Locate every blood parasite and identify its species.
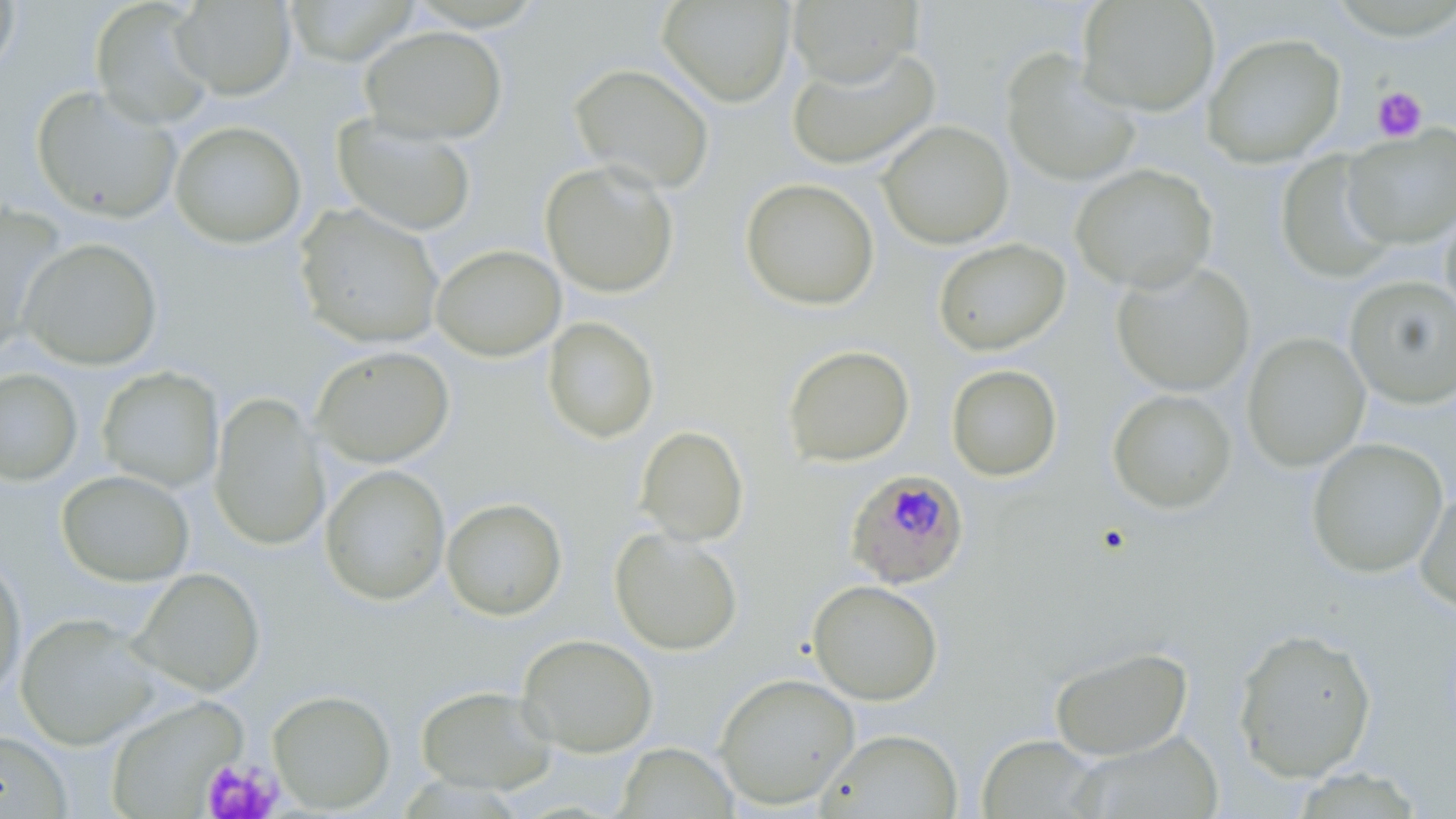
Approximate bounding boxes as (x1, y1, x2, y2) in pixels.
Plasmodium falciparum-infected red blood cells: (845, 469, 971, 590).
No Plasmodium ovale, Plasmodium malariae, Plasmodium vivax, Babesia divergens, or Trypanosoma brucei observed.

Summary:
  - Uninfected red blood cell locations: (0, 0, 21, 82), (90, 0, 216, 130), (657, 0, 795, 107), (787, 0, 922, 88), (170, 1, 297, 100), (1076, 1, 1220, 116), (282, 2, 421, 67), (359, 25, 508, 144), (1202, 31, 1346, 167), (786, 46, 940, 170), (1000, 50, 1142, 187), (569, 63, 715, 194), (30, 85, 182, 224), (332, 115, 477, 236), (169, 120, 307, 249), (877, 120, 1014, 249), (1342, 125, 1456, 249), (1276, 151, 1399, 283), (540, 159, 679, 298), (1069, 163, 1218, 294), (740, 177, 880, 311), (1440, 202, 1456, 325), (294, 204, 445, 350), (1, 205, 66, 356), (18, 238, 163, 370), (933, 238, 1070, 356), (431, 244, 566, 361), (1111, 259, 1255, 397), (1344, 275, 1456, 409), (541, 316, 660, 443), (1242, 332, 1370, 472), (782, 344, 914, 467), (311, 346, 455, 467), (946, 364, 1063, 481), (97, 366, 224, 493), (0, 367, 83, 487), (1107, 388, 1237, 514), (208, 391, 330, 551), (635, 425, 749, 546), (1306, 437, 1449, 578), (319, 464, 451, 606), (56, 470, 195, 586), (1414, 486, 1456, 616), (441, 497, 567, 621), (609, 527, 743, 655), (0, 551, 26, 702), (130, 567, 266, 697), (807, 579, 943, 705), (16, 613, 160, 749), (1232, 627, 1377, 782), (517, 633, 658, 757), (1050, 646, 1192, 761), (714, 672, 859, 810), (415, 684, 557, 794), (267, 689, 396, 813), (105, 696, 249, 817), (817, 728, 964, 818), (0, 730, 72, 817), (1069, 730, 1224, 819), (976, 734, 1105, 819), (615, 742, 738, 818)
  - Platelet locations: (1372, 86, 1428, 143), (203, 757, 284, 819)
  - Slide-level diagnosis: Plasmodium falciparum
  - Preparation: thin blood smear
  - Stain: May-Grünwald-Giemsa
  - Modality: light microscopy
  - Image size: 1456×819 pixels
  - Field of view: single
  - Magnification: 1000x